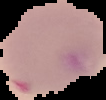 From a thin blood smear. Image is 106×100 pixels. The area outside the segmented cell region is set to black. Result: malaria parasites detected.